Assess this cell for malaria.
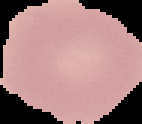

Uninfected.

From a thin blood film. Image is 142×124 pixels. Segmented cell region on a black background.